Identify the preparation type.
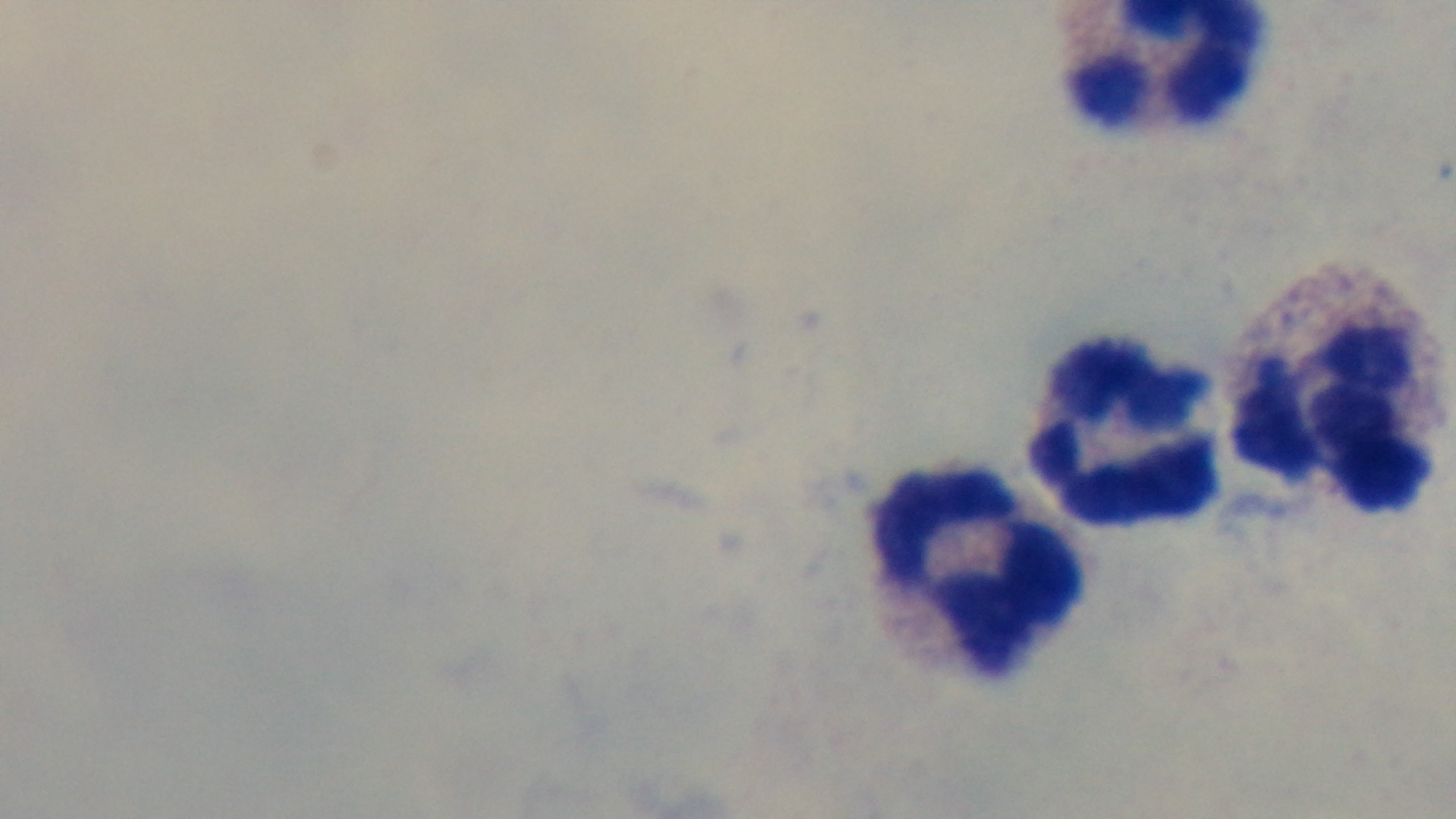
A thick smear.

Summary:
  - Modality: light microscopy
  - Malaria status: uninfected
  - Objective: 100x oil immersion
  - Capture: mounted 4K digital camera
  - Field of view: one from the slide
  - Stain: Giemsa